Report the malaria status of this cell.
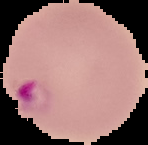

Parasitized.

From a thin blood smear. Image is 148×145 pixels. Segmented cell region on a black background.